Locate platelets.
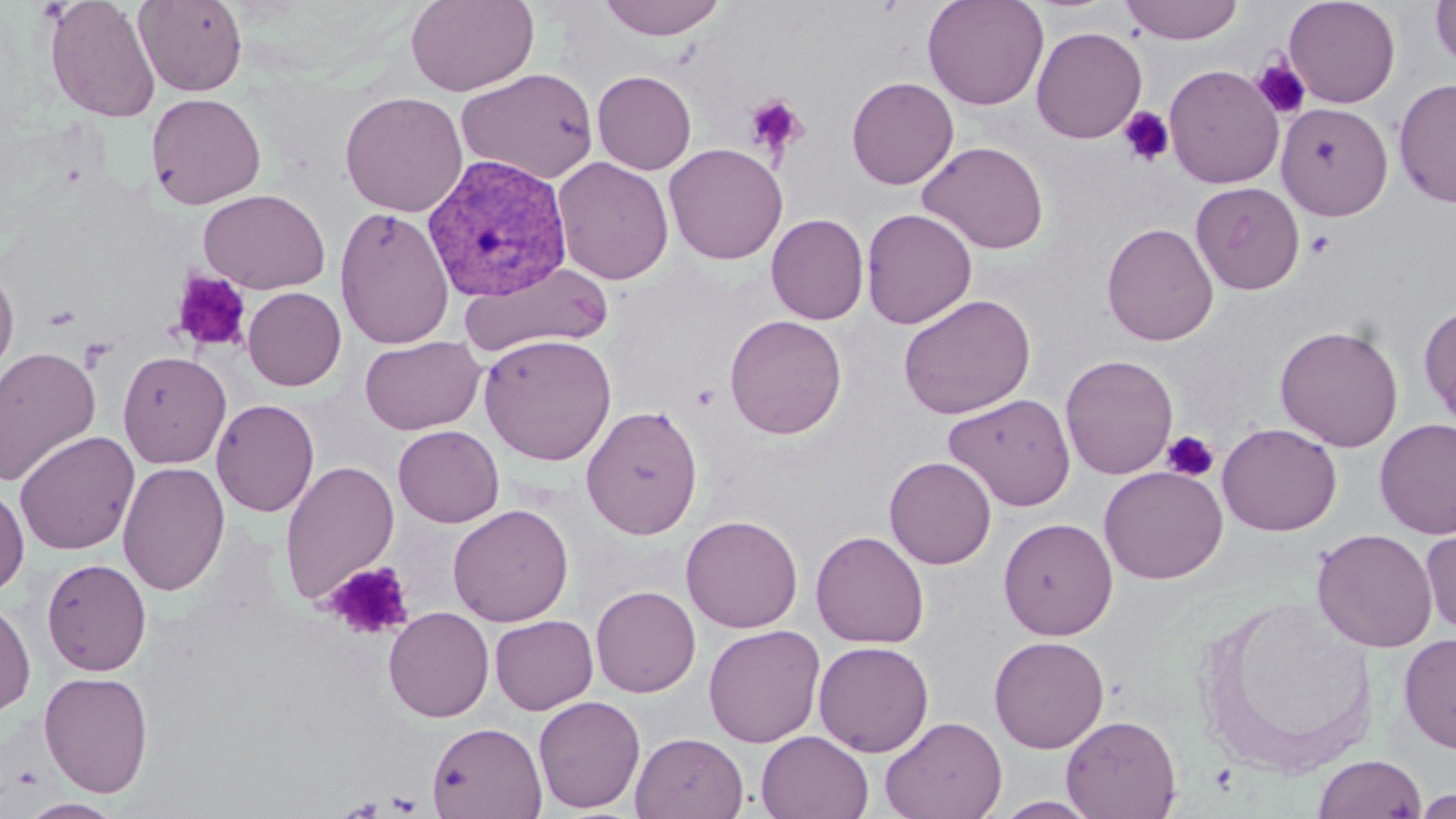
Approximate bounding boxes as (x1,y1)-(x2,y2) corner pairs in pixels.
Platelets: (1251,57)-(1312,120), (743,94)-(809,159), (1118,106)-(1175,166), (170,270)-(252,354), (79,337)-(116,372), (691,383)-(720,410), (1162,429)-(1220,483), (325,562)-(414,641), (386,792)-(424,815).

Summary:
  - Uninfected red blood cell locations: (44,0)-(160,123), (406,0)-(538,96), (597,0)-(729,41), (922,0)-(1049,111), (1121,0)-(1243,44), (1283,0)-(1401,108), (134,1)-(248,96), (1430,1)-(1456,72), (1031,26)-(1147,143), (1164,64)-(1285,189), (456,68)-(599,184), (592,70)-(696,174), (846,76)-(959,189), (1394,78)-(1456,208), (340,91)-(468,217), (145,92)-(266,209), (1276,102)-(1393,220), (917,140)-(1050,255), (664,143)-(788,264), (553,156)-(674,285), (1190,182)-(1305,295), (198,188)-(331,294), (334,206)-(455,350), (861,208)-(978,329), (766,214)-(869,325), (1101,222)-(1219,346), (0,261)-(19,385), (458,262)-(615,358), (243,287)-(346,391), (898,294)-(1036,419), (1419,302)-(1456,428), (724,314)-(847,439), (1275,324)-(1403,451), (479,333)-(617,465), (360,335)-(486,435), (0,346)-(102,486), (117,350)-(231,468), (1060,354)-(1178,479), (944,392)-(1076,512), (211,398)-(320,517), (581,404)-(703,539), (1374,418)-(1456,539), (1217,422)-(1341,536), (393,425)-(504,527), (14,431)-(140,555), (884,456)-(996,569), (279,460)-(400,605), (117,461)-(230,597), (1099,465)-(1227,584), (0,483)-(29,598), (448,504)-(574,627), (681,515)-(803,633), (998,517)-(1118,640), (1421,523)-(1456,635), (1311,528)-(1437,653), (810,530)-(929,649), (41,558)-(151,676), (591,585)-(701,698), (1195,595)-(1379,779), (0,596)-(36,719), (383,606)-(494,722), (490,614)-(598,714), (703,624)-(826,747), (1399,632)-(1456,754), (989,635)-(1109,753), (814,640)-(934,757), (39,670)-(154,798), (533,695)-(646,814), (1061,714)-(1181,819), (880,716)-(1007,819), (426,721)-(546,819), (756,731)-(874,818), (631,732)-(749,819), (1313,753)-(1426,818), (1414,788)-(1456,818), (991,796)-(1104,818), (19,798)-(127,818)
  - Plasmodium vivax-infected red blood cell locations: (422,153)-(574,302)
  - Slide-level diagnosis: Plasmodium vivax
  - Modality: optical microscopy
  - Magnification: 1000x
  - Field of view: one of a larger specimen
  - Preparation: thin blood smear
  - Stain: May-Grünwald-Giemsa
  - Image size: 1456×819 pixels